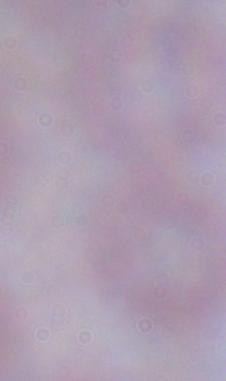

Summary:
  - Modality: photomicrograph
  - Magnification: 1000x
  - Identification: trypanosome